Locate every Plasmodium ovale-infected red blood cell.
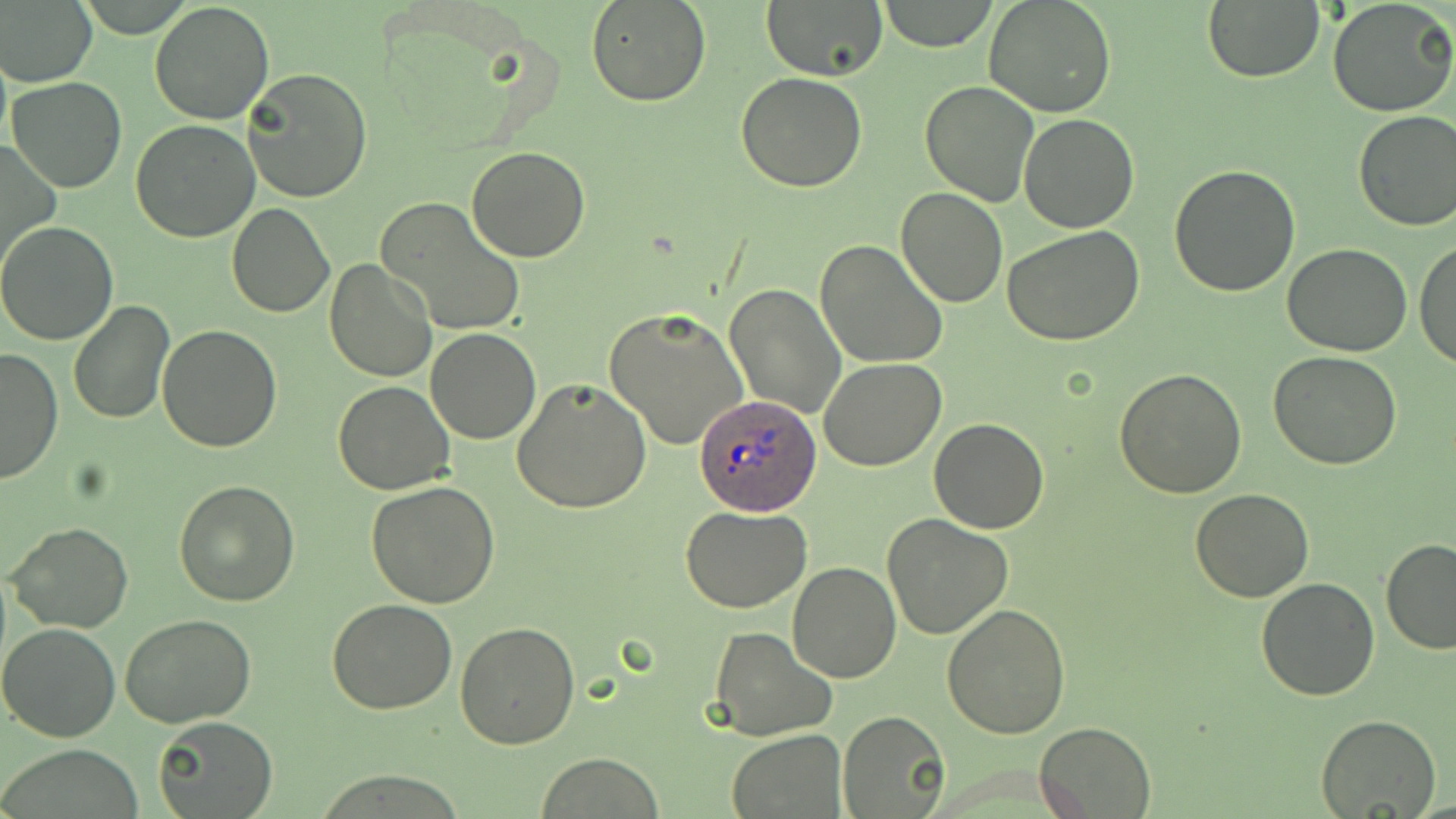
Approximate bounding boxes as (x1,y1)-(x2,y2) corner pairs in pixels.
Plasmodium ovale-infected red blood cells: (696,394)-(823,514).

Summary:
  - Uninfected red blood cell locations: (1,0)-(97,87), (149,0)-(275,123), (585,0)-(712,108), (761,0)-(887,82), (878,0)-(998,51), (984,0)-(1117,118), (1201,0)-(1325,83), (1328,0)-(1456,117), (243,69)-(372,202), (735,72)-(868,192), (6,76)-(128,192), (918,79)-(1039,208), (1353,109)-(1456,231), (1018,113)-(1139,233), (131,118)-(259,242), (1,137)-(60,277), (466,145)-(593,263), (1168,165)-(1301,298), (895,187)-(1007,308), (375,196)-(527,337), (226,202)-(335,318), (0,222)-(119,346), (1002,226)-(1145,346), (815,239)-(947,371), (1415,240)-(1456,372), (1282,242)-(1411,356), (324,259)-(439,383), (724,283)-(845,420), (69,301)-(173,425), (604,307)-(751,451), (156,324)-(284,452), (425,327)-(541,444), (1,347)-(62,484), (1268,351)-(1402,471), (820,359)-(948,472), (1115,367)-(1248,499), (512,378)-(651,513), (333,380)-(454,494), (928,418)-(1051,533), (174,479)-(302,606), (366,483)-(500,609), (1191,488)-(1313,602), (681,505)-(812,614), (881,514)-(1013,639), (6,522)-(133,633), (1379,539)-(1456,655), (787,561)-(902,683), (1256,576)-(1379,700), (327,600)-(457,715), (942,603)-(1072,739), (120,613)-(258,729), (0,622)-(121,742), (456,623)-(581,749), (710,626)-(837,742), (840,710)-(951,819), (1314,714)-(1440,819), (152,716)-(278,819), (1033,720)-(1157,817), (728,730)-(845,817), (537,753)-(664,818)
  - Slide-level diagnosis: Plasmodium ovale
  - Stain: May-Grünwald-Giemsa
  - Field of view: single
  - Magnification: 1000x
  - Modality: optical microscopy
  - Preparation: thin blood film
  - Image size: 1456×819 pixels